Locate every Plasmodium ovale-infected red blood cell.
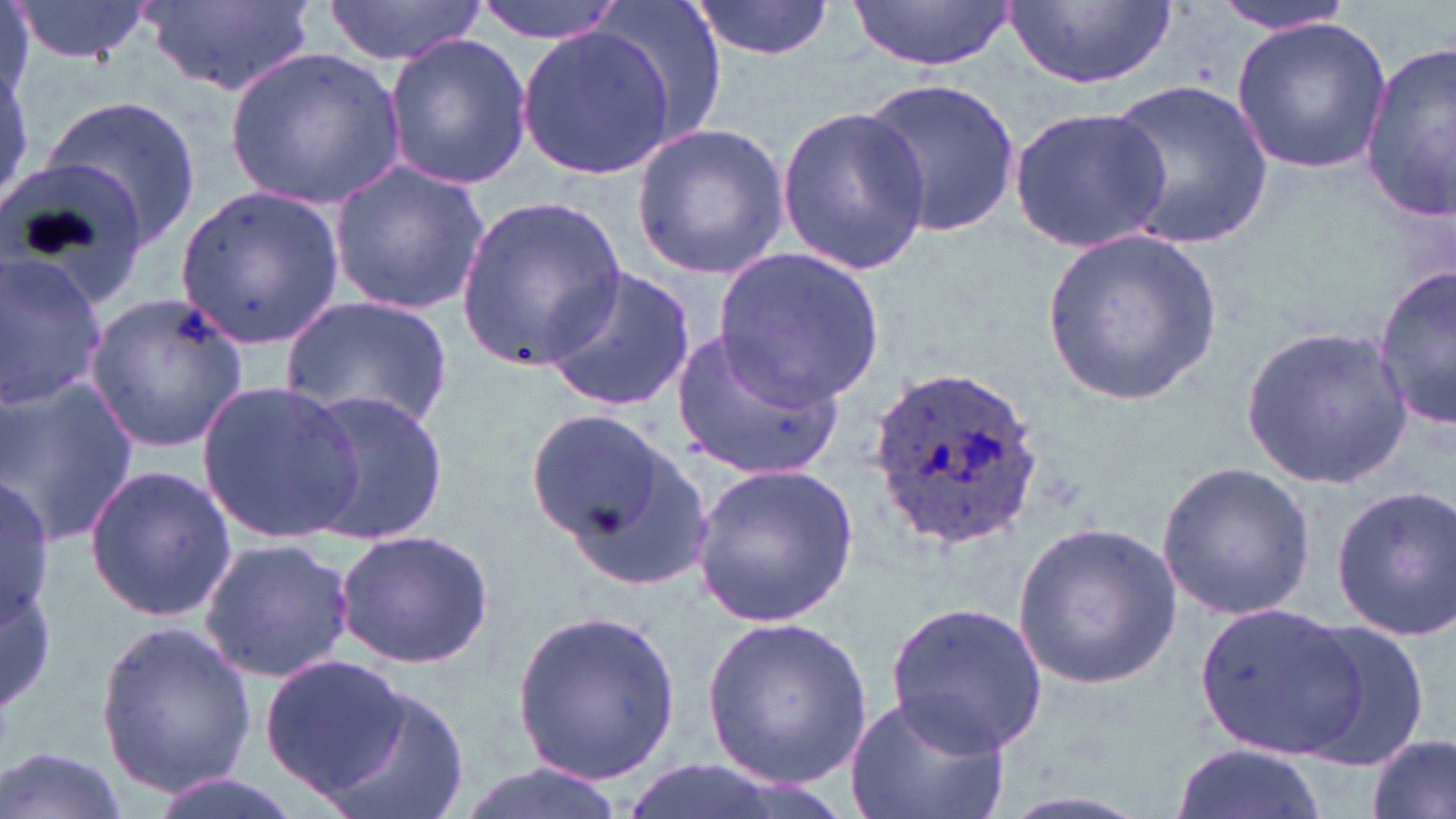
Approximate bounding boxes as [x1, y1, x2, y2] in pixels.
Plasmodium ovale-infected red blood cells: [868, 368, 1044, 541].

Summary:
  - Uninfected red blood cell locations: [8, 0, 157, 65], [144, 0, 318, 99], [321, 0, 493, 66], [474, 0, 632, 43], [594, 0, 733, 149], [687, 0, 837, 62], [1000, 0, 1179, 93], [849, 1, 1017, 73], [1212, 1, 1360, 35], [1232, 16, 1391, 175], [514, 22, 678, 178], [382, 34, 533, 190], [1357, 43, 1456, 222], [227, 47, 404, 207], [862, 78, 1022, 240], [1106, 79, 1277, 249], [38, 93, 203, 249], [773, 102, 930, 277], [1007, 105, 1175, 254], [631, 124, 788, 277], [328, 160, 491, 316], [0, 162, 152, 314], [177, 183, 344, 346], [454, 195, 626, 372], [1044, 230, 1221, 407], [714, 246, 885, 407], [0, 254, 111, 406], [1374, 266, 1456, 432], [542, 267, 697, 412], [84, 293, 247, 454], [284, 296, 455, 434], [668, 323, 843, 482], [1241, 325, 1413, 489], [3, 374, 141, 547], [196, 381, 365, 541], [299, 387, 451, 547], [522, 406, 679, 557], [1155, 460, 1317, 622], [691, 462, 859, 626], [84, 465, 234, 623], [0, 476, 55, 634], [1328, 483, 1456, 642], [1009, 521, 1183, 690], [334, 529, 495, 668], [199, 537, 356, 684], [1195, 601, 1366, 758], [884, 603, 1049, 756], [512, 606, 681, 783], [702, 615, 871, 788], [1295, 615, 1429, 769], [93, 616, 256, 801], [259, 653, 411, 800], [314, 679, 470, 819], [844, 691, 1011, 819], [1368, 733, 1455, 819], [1169, 740, 1325, 819], [0, 745, 131, 819], [447, 764, 633, 819], [146, 772, 309, 819]
  - Slide-level diagnosis: Plasmodium ovale
  - Image size: 1456×819 pixels
  - Magnification: 1000x
  - Stain: May-Grünwald-Giemsa
  - Preparation: thin blood smear
  - Modality: light microscopy
  - Field of view: one of a larger specimen